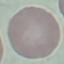

Summary:
  - Malaria status: uninfected
  - Capture: smartphone through the microscope eyepiece
  - Stain: Giemsa
  - Image type: cell patch, automatically extracted from a larger field of view and resized to 64 × 64 pixels
  - Preparation: thin blood film